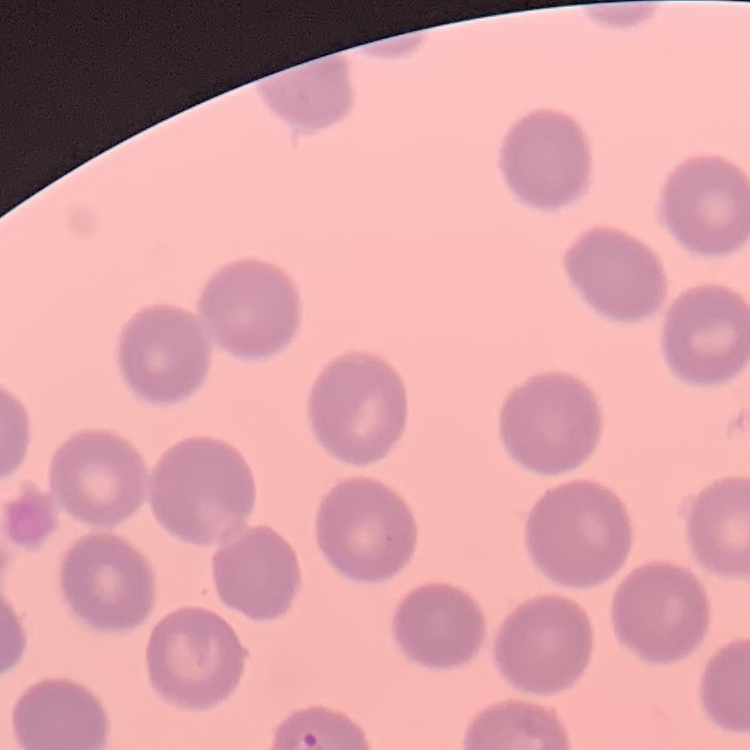

red_blood_cell_morphology: no rouleaux formation
stain: Field's or Giemsa
preparation: thin blood smear
image_type: square crop of a larger photomicrograph